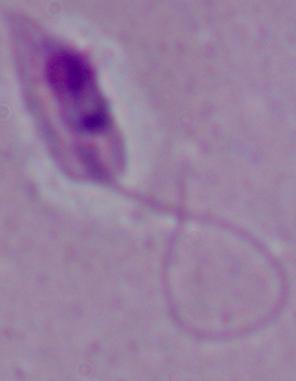
modality = micrograph
identification = Leishmania
magnification = 1000x